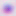

modality = photomicrograph
magnification = 400x
identification = Toxoplasma gondii